Name the blood parasite species.
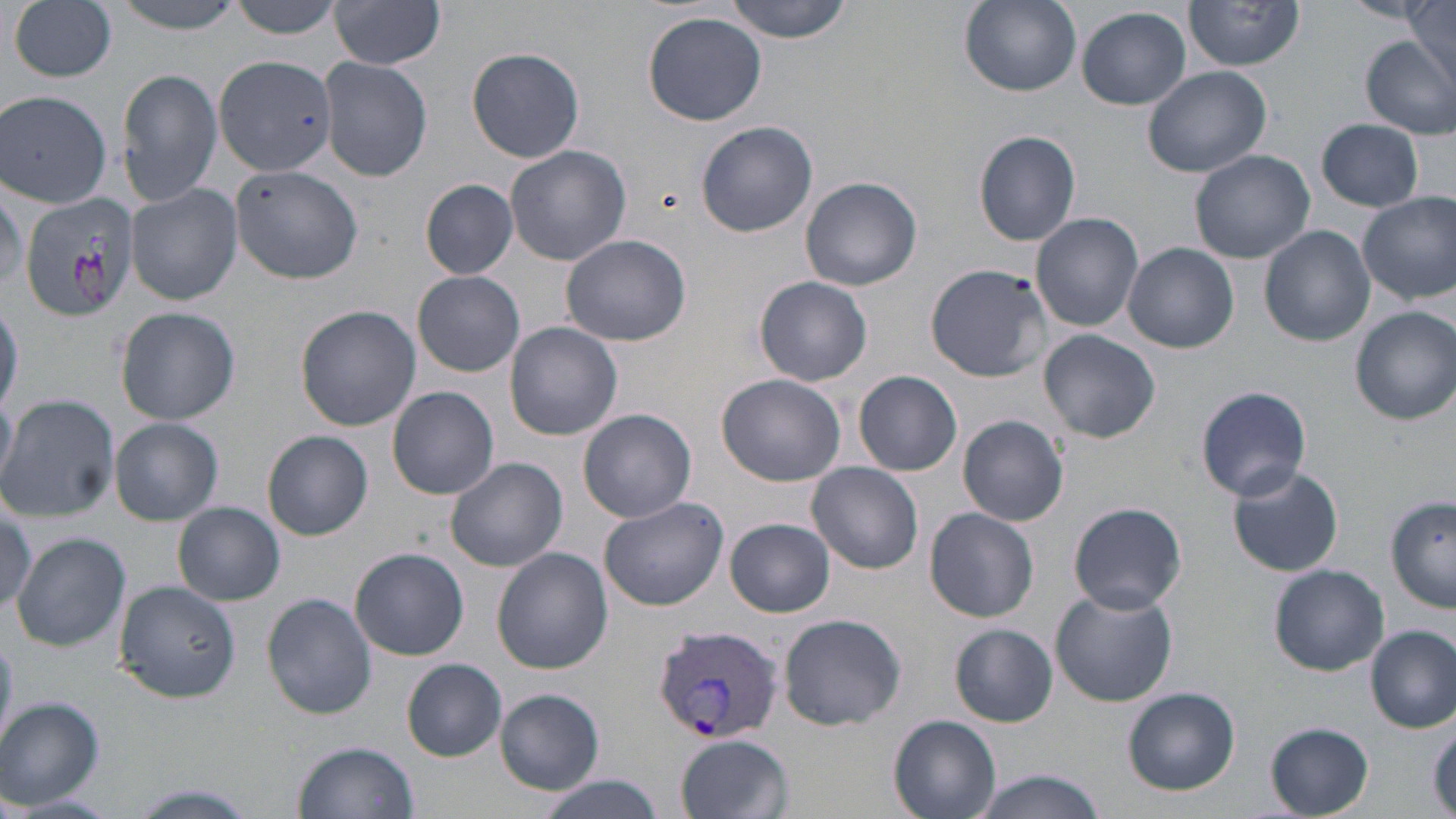
Plasmodium vivax.

Summary:
  - Coordinate format: approximate bounding boxes as (x1, y1, x2, y2) in pixels
  - Plasmodium vivax-infected red blood cell locations: (651, 624, 786, 744)
  - Uninfected red blood cell locations: (106, 0, 252, 33), (225, 0, 347, 38), (724, 0, 853, 42), (1185, 0, 1305, 70), (1404, 0, 1454, 77), (9, 1, 118, 83), (960, 1, 1081, 96), (1343, 1, 1433, 26), (331, 3, 445, 71), (1077, 6, 1191, 110), (643, 12, 767, 126), (1361, 35, 1455, 138), (467, 47, 585, 163), (215, 56, 336, 175), (320, 57, 433, 182), (116, 66, 223, 207), (1142, 66, 1275, 179), (1, 89, 114, 209), (1317, 118, 1425, 211), (697, 120, 817, 237), (974, 128, 1081, 247), (505, 145, 632, 266), (1189, 148, 1314, 264), (229, 161, 366, 283), (801, 176, 922, 291), (418, 180, 520, 278), (125, 182, 243, 306), (20, 189, 140, 318), (1357, 190, 1456, 305), (1031, 212, 1144, 332), (1260, 226, 1375, 348), (561, 234, 692, 347), (1123, 243, 1239, 353), (925, 264, 1051, 382), (413, 271, 524, 378), (755, 276, 873, 386), (0, 296, 23, 418), (295, 304, 420, 430), (115, 306, 240, 424), (1350, 307, 1456, 425), (505, 321, 624, 441), (1038, 329, 1161, 443), (854, 370, 963, 476), (718, 374, 845, 486), (387, 386, 499, 500), (1197, 386, 1314, 500), (0, 393, 16, 481), (0, 394, 119, 523), (579, 409, 696, 523), (957, 415, 1069, 526), (110, 418, 223, 525), (262, 430, 374, 540), (445, 456, 567, 573), (807, 462, 923, 575), (1225, 464, 1345, 577), (598, 495, 730, 610), (1386, 498, 1455, 613), (0, 499, 36, 616), (173, 502, 286, 606), (1067, 502, 1189, 614), (925, 508, 1039, 622), (725, 518, 835, 617), (11, 533, 133, 653), (350, 548, 469, 659), (492, 549, 613, 676), (1269, 564, 1389, 676), (112, 580, 241, 702), (1050, 587, 1178, 706), (262, 593, 377, 719), (778, 612, 908, 730), (951, 623, 1057, 727), (1367, 624, 1455, 732), (403, 659, 507, 760), (494, 687, 605, 795), (1124, 687, 1240, 795), (0, 697, 104, 808), (889, 715, 1000, 819), (1429, 719, 1456, 816), (1264, 722, 1375, 818), (676, 733, 792, 818), (294, 739, 421, 819), (967, 770, 1107, 819), (533, 774, 667, 819), (122, 784, 260, 819), (10, 793, 114, 818)
  - Magnification: 1000x
  - Stain: May-Grünwald-Giemsa
  - Preparation: thin blood smear
  - Image size: 1456×819 pixels
  - Modality: optical microscopy
  - Field of view: single